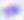
Summary:
  - Magnification: 400x
  - Modality: photomicrograph
  - Identification: Toxoplasma gondii